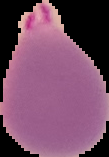

preparation = thin blood smear
image size = 109×157 pixels
image type = segmented cell region with the area outside set to black
malaria status = parasitized